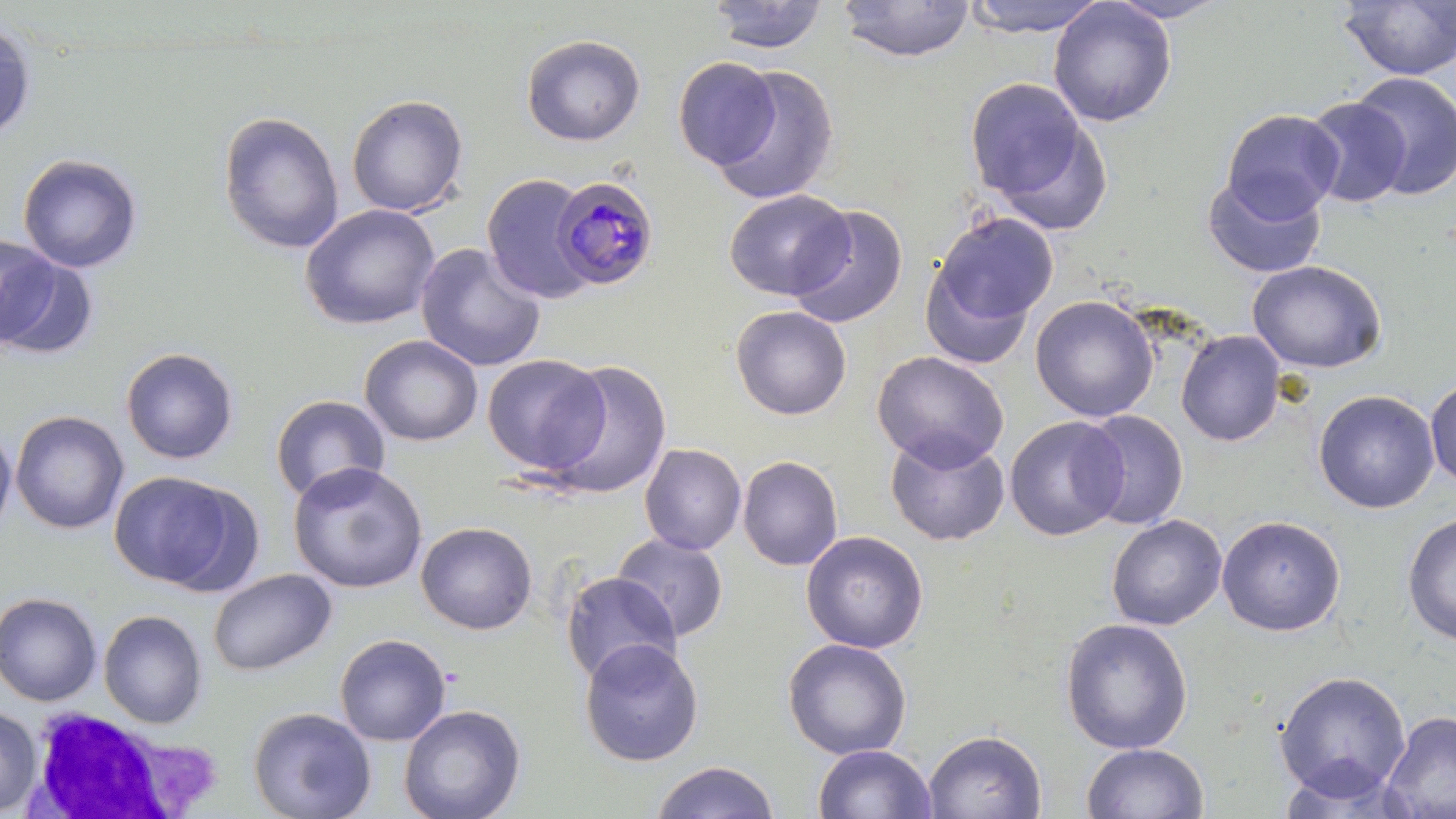 Approximate bounding boxes as (x1, y1, x2, y2) in pixels. White blood cell locations: (24, 708, 194, 817). Uninfected red blood cell locations: (707, 0, 829, 54), (961, 0, 1109, 37), (1104, 0, 1233, 23), (838, 1, 974, 62), (1048, 1, 1176, 127), (1337, 1, 1456, 81), (0, 17, 36, 142), (521, 34, 646, 146), (673, 56, 780, 169), (709, 64, 840, 205), (1349, 71, 1456, 200), (964, 77, 1099, 216), (346, 94, 469, 217), (1302, 97, 1411, 208), (1221, 109, 1344, 221), (217, 110, 344, 254), (17, 153, 143, 273), (481, 173, 593, 303), (1202, 173, 1327, 279), (724, 189, 854, 301), (299, 203, 441, 330), (785, 204, 910, 328), (926, 211, 1059, 339), (415, 243, 546, 372), (0, 250, 100, 360), (919, 256, 1039, 373), (1247, 261, 1387, 374), (1030, 295, 1159, 422), (730, 305, 852, 420), (1176, 330, 1286, 446), (360, 334, 482, 446), (121, 347, 239, 464), (871, 350, 1009, 471), (482, 354, 609, 475), (542, 359, 673, 499), (1425, 374, 1456, 489), (1313, 389, 1440, 514), (269, 394, 391, 504), (1077, 409, 1189, 530), (10, 410, 129, 534), (1004, 416, 1128, 542), (0, 422, 17, 541), (884, 430, 1010, 546), (639, 443, 746, 555), (737, 455, 843, 571), (288, 462, 429, 594), (108, 470, 254, 593), (1402, 512, 1456, 645), (1106, 514, 1227, 631), (1217, 515, 1346, 636), (415, 522, 538, 635), (801, 531, 928, 653), (611, 533, 730, 642), (208, 568, 337, 677), (559, 571, 683, 685), (0, 592, 102, 707), (98, 609, 208, 728), (1059, 617, 1194, 754), (334, 633, 451, 746), (579, 638, 704, 767), (782, 638, 912, 760), (1274, 670, 1411, 800), (398, 703, 527, 819), (0, 705, 42, 817), (247, 707, 376, 819), (1380, 710, 1456, 819), (923, 729, 1045, 818), (1081, 743, 1210, 818), (813, 744, 937, 819), (649, 760, 781, 819). Plasmodium malariae-infected red blood cell locations: (550, 174, 660, 290). Slide-level diagnosis: Plasmodium malariae. Thin blood film. Single field of view. Image is 1456×819 pixels. Light microscopy. Captured at 1000x magnification. May-Grünwald-Giemsa stain.